Mark where white blood cells are.
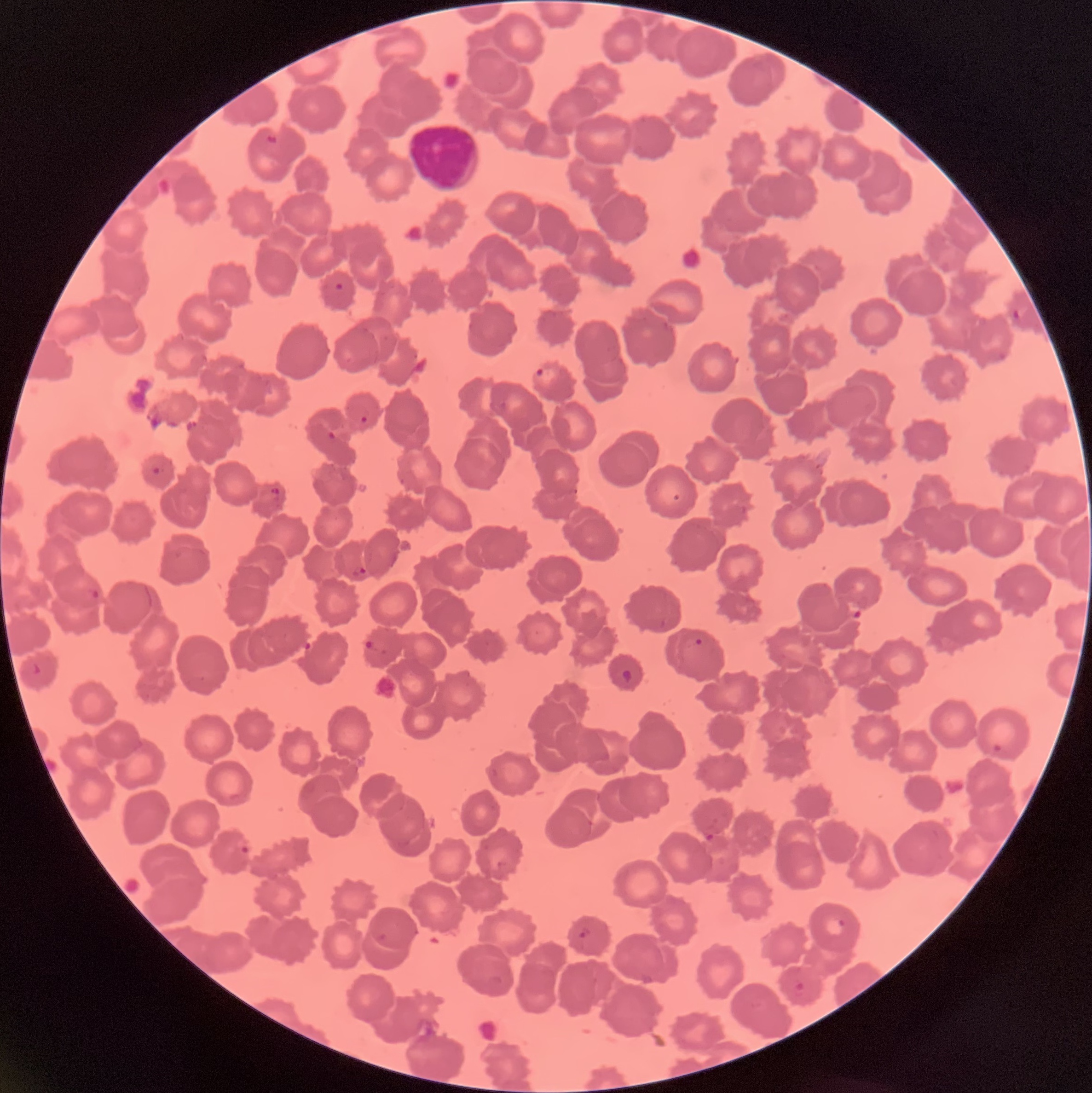

Approximate bounding boxes as named x1/y1/x2/y2 corners in pixels.
White blood cells: (x1=411, y1=125, x2=485, y2=191).

Summary:
  - Plasmodium parasite locations: (x1=263, y1=134, x2=278, y2=146), (x1=334, y1=282, x2=344, y2=291), (x1=1012, y1=308, x2=1028, y2=319), (x1=534, y1=366, x2=556, y2=385), (x1=360, y1=414, x2=368, y2=423), (x1=327, y1=432, x2=338, y2=439), (x1=152, y1=467, x2=166, y2=475), (x1=271, y1=486, x2=281, y2=496), (x1=355, y1=567, x2=367, y2=577), (x1=89, y1=589, x2=100, y2=599), (x1=695, y1=638, x2=704, y2=646), (x1=363, y1=641, x2=375, y2=650), (x1=29, y1=663, x2=42, y2=675), (x1=622, y1=670, x2=632, y2=683), (x1=993, y1=744, x2=1006, y2=753), (x1=706, y1=833, x2=714, y2=841), (x1=239, y1=845, x2=251, y2=855), (x1=824, y1=917, x2=845, y2=936), (x1=578, y1=926, x2=592, y2=939), (x1=793, y1=983, x2=805, y2=994)
  - Image size: 1092×1093 pixels
  - Red blood cell morphology: rouleaux formation
  - Preparation: thin blood smear
  - Modality: light microscopy